Report the malaria status of this cell.
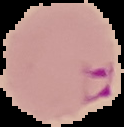
It is parasitized.

Summary:
  - Image size: 124×127 pixels
  - Preparation: thin blood smear
  - Image type: segmented cell region with the area outside set to black